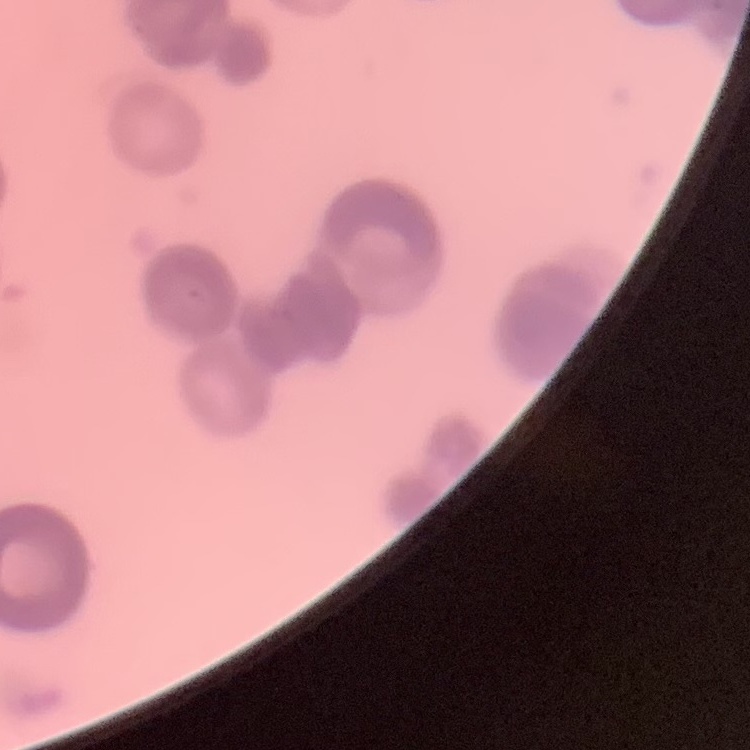
Summary:
  - Erythrocyte morphology: rouleaux formation
  - Image type: square crop of a larger photomicrograph
  - Stain: Field's or Giemsa
  - Preparation: thin peripheral smear